Locate every blood parasite and identify its species.
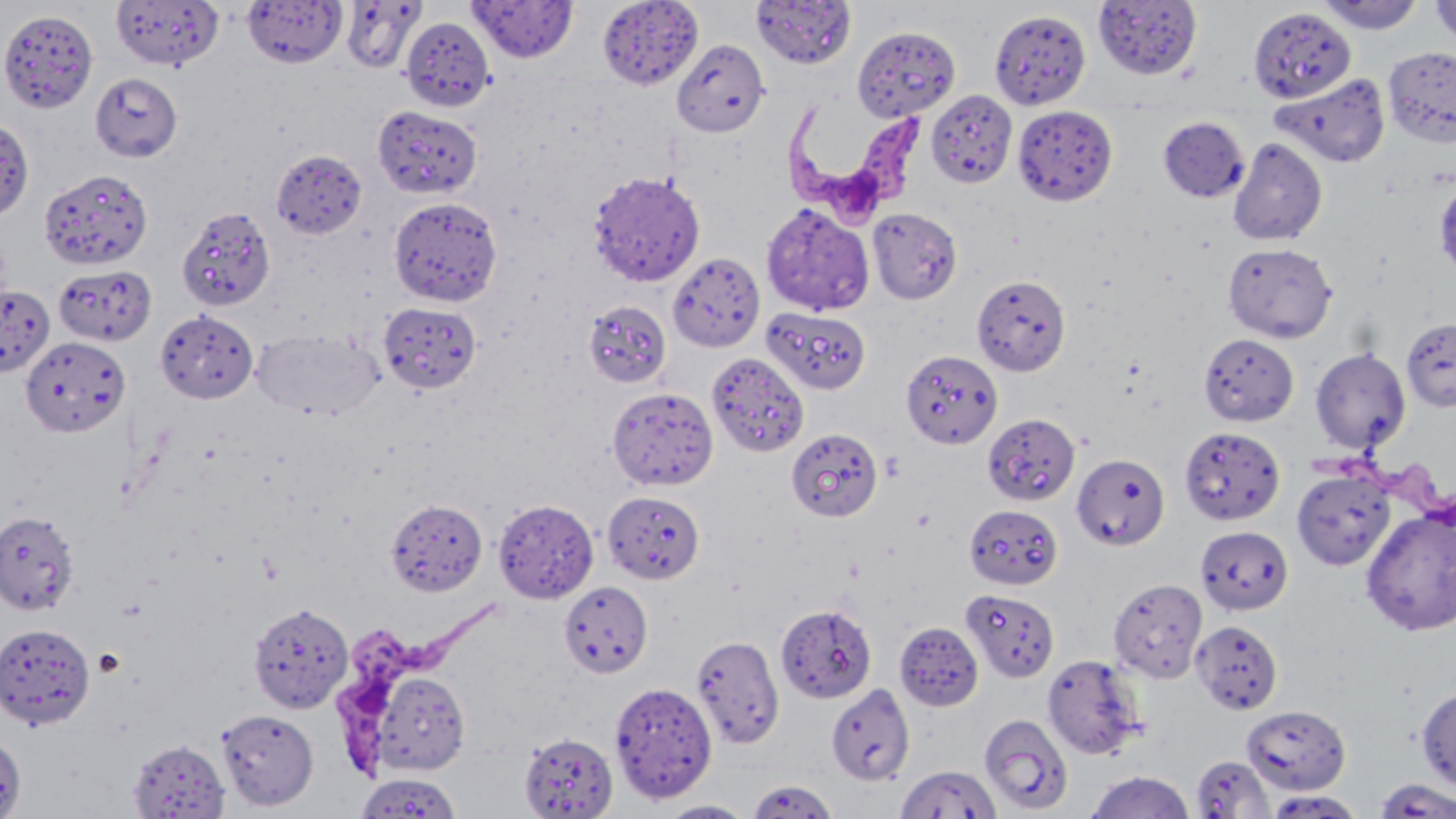

Approximate bounding boxes as (x1,y1)-(x2,y2) corner pairs in pixels.
Trypanosoma brucei: (783,101)-(928,222), (1315,440)-(1453,544), (336,599)-(499,777).
No Plasmodium falciparum, Plasmodium ovale, Plasmodium malariae, Plasmodium vivax, or Babesia divergens observed.

Summary:
  - Uninfected red blood cell locations: (242,0)-(347,67), (340,0)-(425,73), (469,0)-(577,63), (597,0)-(703,90), (750,0)-(857,69), (1314,0)-(1425,33), (1430,0)-(1456,46), (111,1)-(222,70), (1093,1)-(1202,79), (1249,7)-(1356,104), (0,9)-(99,114), (990,9)-(1090,111), (401,16)-(495,111), (852,25)-(960,122), (672,39)-(770,137), (1383,45)-(1456,148), (91,72)-(182,162), (1271,73)-(1390,168), (926,90)-(1018,188), (372,105)-(481,199), (1012,105)-(1118,205), (1158,116)-(1249,202), (0,119)-(34,221), (1228,137)-(1327,245), (271,148)-(367,238), (39,167)-(153,270), (588,170)-(705,287), (1433,177)-(1456,281), (388,196)-(502,307), (761,202)-(874,316), (177,206)-(276,312), (867,208)-(962,304), (1223,242)-(1337,343), (668,252)-(765,351), (53,264)-(156,346), (971,274)-(1070,376), (0,284)-(54,377), (583,300)-(672,388), (379,302)-(481,393), (762,307)-(871,395), (155,309)-(258,403), (1401,317)-(1456,413), (251,326)-(383,421), (1199,333)-(1299,426), (20,335)-(130,438), (1310,347)-(1411,454), (901,350)-(1001,448), (707,351)-(809,458), (608,387)-(718,491), (983,413)-(1080,506), (1179,426)-(1284,526), (786,428)-(882,522), (1072,453)-(1170,549), (1292,468)-(1394,570), (602,491)-(705,584), (493,498)-(598,603), (385,499)-(486,595), (964,504)-(1063,590), (1360,506)-(1456,636), (0,510)-(79,616), (1196,525)-(1293,615), (1108,578)-(1207,683), (559,581)-(653,677), (961,588)-(1059,682), (248,603)-(353,714), (776,604)-(877,703), (1191,620)-(1283,714), (894,621)-(983,711), (1,624)-(95,730), (691,634)-(784,749), (1042,653)-(1147,760), (370,670)-(471,776), (609,680)-(717,803), (826,683)-(914,785), (1416,685)-(1456,792), (1241,704)-(1350,794), (217,708)-(318,810), (979,714)-(1074,815), (0,732)-(27,819), (520,732)-(618,818), (128,739)-(230,818), (1191,754)-(1274,818), (895,768)-(1000,819), (1086,770)-(1195,819), (354,772)-(461,818), (1373,778)-(1456,818), (746,779)-(839,819), (1264,790)-(1366,818), (656,800)-(755,818)
  - Slide-level diagnosis: Trypanosoma brucei
  - Magnification: 1000x
  - Image size: 1456×819 pixels
  - Preparation: thin blood smear
  - Stain: May-Grünwald-Giemsa
  - Field of view: single
  - Modality: optical microscopy